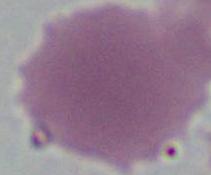
modality: photomicrograph
magnification: 1000x
identification: erythrocyte